Identify the blood parasite species.
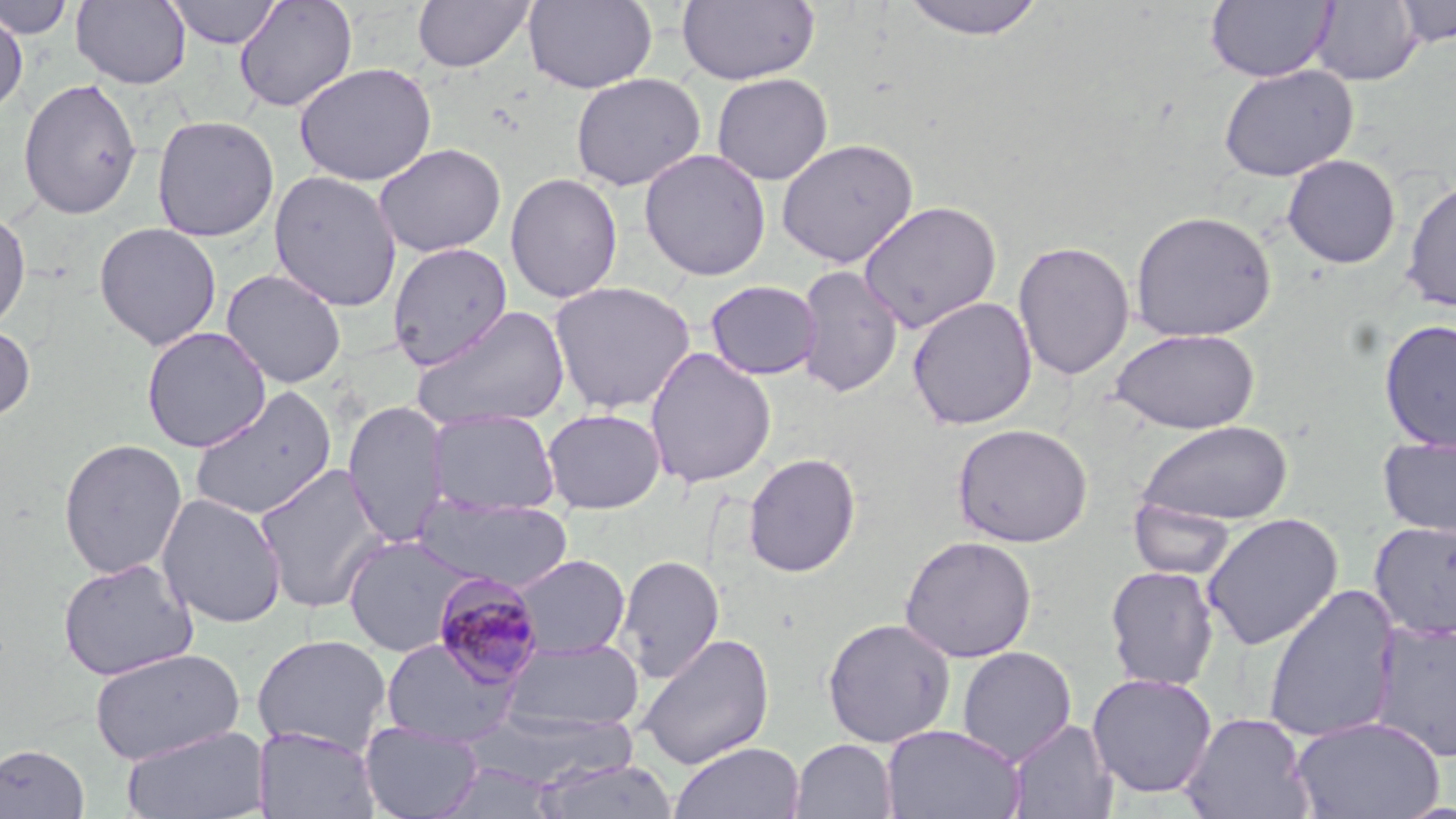

Plasmodium malariae.

Approximate bounding boxes as [x1, y1, x2, y2] in pixels. Plasmodium malariae-infected red blood cell locations: [430, 572, 545, 688]. Uninfected red blood cell locations: [1, 0, 76, 39], [71, 0, 191, 89], [166, 0, 281, 48], [233, 0, 358, 113], [412, 0, 536, 73], [524, 0, 657, 93], [676, 0, 821, 85], [898, 0, 1048, 41], [1205, 0, 1335, 82], [1310, 1, 1421, 87], [1394, 1, 1456, 47], [0, 9, 28, 116], [294, 62, 438, 186], [1218, 64, 1358, 181], [570, 73, 706, 191], [711, 73, 833, 185], [17, 78, 143, 219], [151, 114, 280, 242], [776, 137, 919, 268], [373, 143, 506, 258], [639, 149, 772, 281], [1281, 154, 1401, 269], [268, 169, 402, 312], [504, 172, 623, 303], [1401, 177, 1456, 313], [858, 200, 1003, 334], [0, 206, 31, 332], [1129, 209, 1277, 342], [94, 222, 222, 350], [1013, 239, 1135, 381], [387, 241, 513, 370], [794, 263, 904, 398], [221, 269, 347, 388], [704, 279, 822, 380], [548, 280, 697, 414], [906, 296, 1037, 430], [411, 305, 571, 432], [1378, 318, 1456, 452], [0, 323, 36, 423], [141, 326, 272, 453], [1111, 328, 1261, 434], [644, 347, 777, 489], [189, 386, 337, 522], [343, 400, 449, 547], [541, 408, 666, 513], [426, 409, 560, 517], [1136, 420, 1294, 526], [952, 423, 1093, 547], [1377, 435, 1456, 538], [57, 437, 187, 580], [742, 452, 861, 577], [253, 462, 391, 613], [156, 492, 288, 629], [416, 496, 571, 591], [1128, 497, 1237, 581], [1201, 512, 1343, 651], [1368, 520, 1456, 640], [342, 533, 478, 658], [898, 535, 1038, 663], [616, 553, 725, 684], [510, 554, 631, 659], [57, 558, 199, 681], [1105, 564, 1221, 691], [1262, 584, 1402, 743], [821, 617, 957, 748], [1369, 618, 1456, 763], [637, 632, 775, 770], [251, 633, 392, 755], [379, 637, 521, 746], [502, 638, 645, 734], [956, 646, 1076, 766], [89, 647, 246, 765], [1087, 673, 1217, 799], [467, 709, 640, 789], [1180, 712, 1315, 819], [1290, 716, 1446, 819], [1007, 718, 1118, 818], [359, 722, 485, 819], [121, 724, 268, 819], [881, 724, 1025, 818], [254, 726, 379, 819], [789, 739, 897, 819], [670, 741, 805, 819], [0, 742, 90, 818], [533, 758, 681, 819], [427, 763, 563, 819]. May-Grünwald-Giemsa-stained preparation. Thin blood film. Optical microscopy. Single field of view. 1000x magnification. Image is 1456×819 pixels.